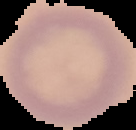 Result: no malaria parasites detected. Cell region segmented out of the field of view; the surrounding area is masked to black. From a thin blood film. Image is 136×130 pixels.